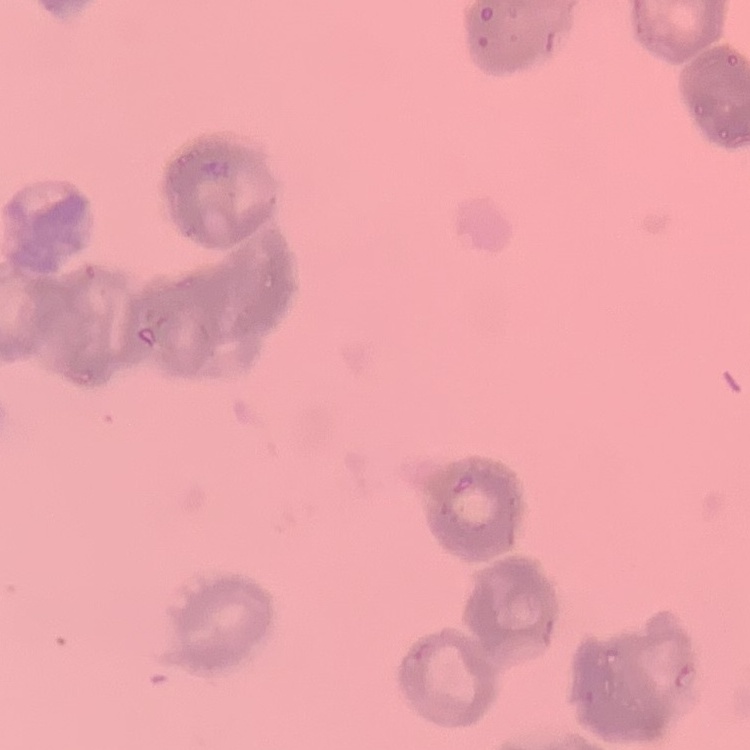
Summary:
  - Red blood cell morphology: rouleaux formation
  - Stain: Field's or Giemsa
  - Preparation: thin blood film
  - Image type: one tile cut from a larger photomicrograph